State which parasite is depicted.
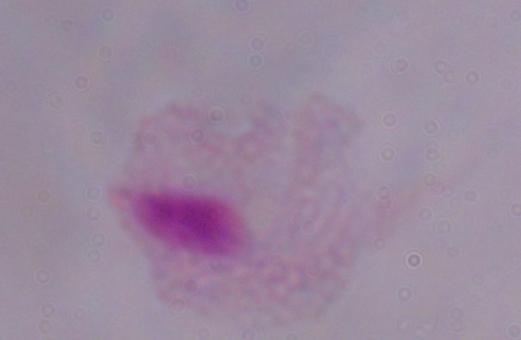
This is a trichomonad.

Captured at 1000x magnification. Micrograph.